State which parasite is depicted.
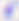

Toxoplasma gondii.

Micrograph. 400x magnification.